Look for Plasmodium parasites.
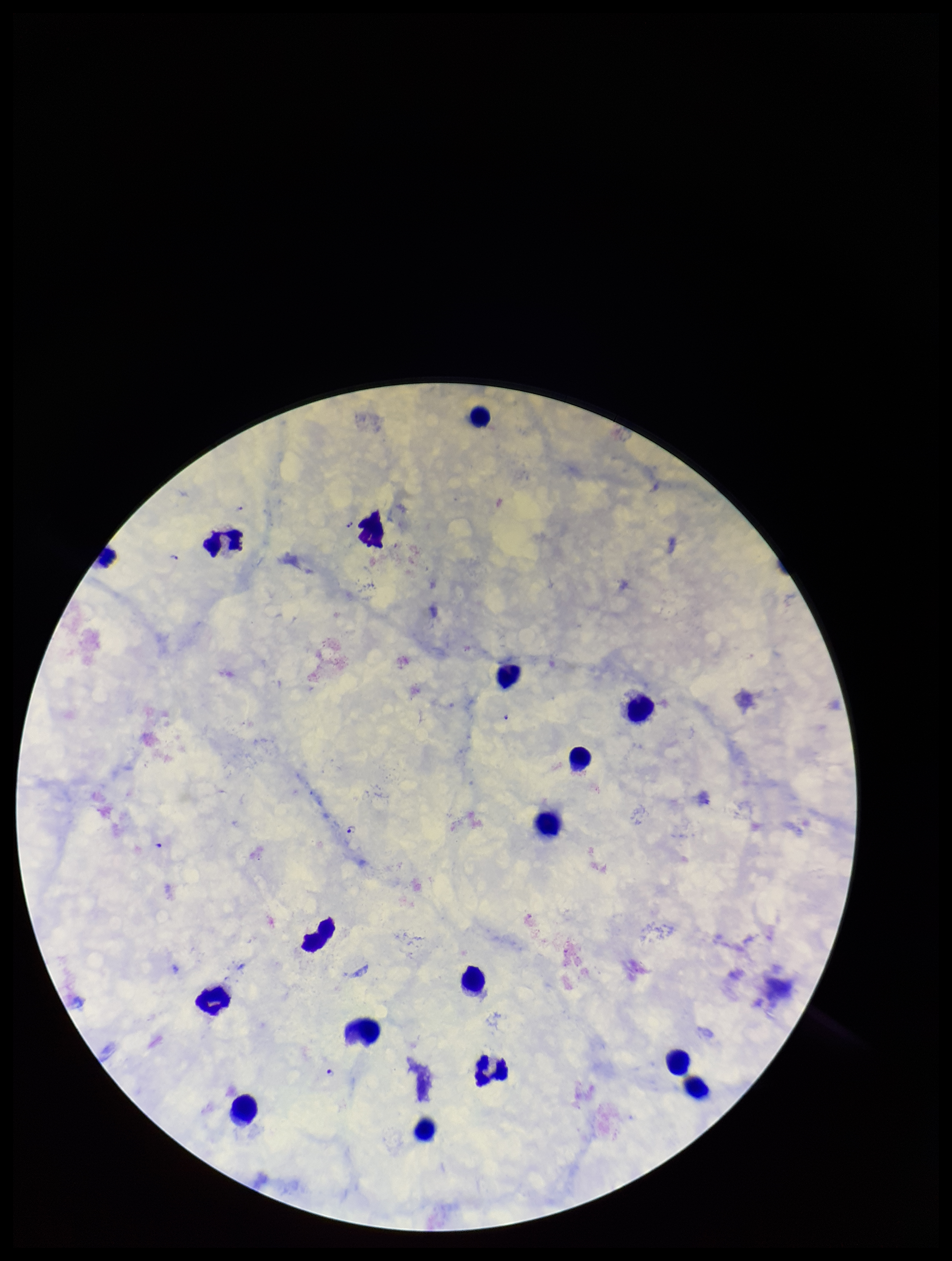
Identified.

Summary:
  - Image size: 952×1261 pixels
  - Preparation: thick blood smear
  - Patient malaria status: infected
  - Leukocyte count: 17
  - Stain: Giemsa
  - Field of view: one from this slide
  - Species reported for this patient: Plasmodium falciparum
  - Capture: smartphone photograph through the microscope eyepiece
  - Parasite count: 4